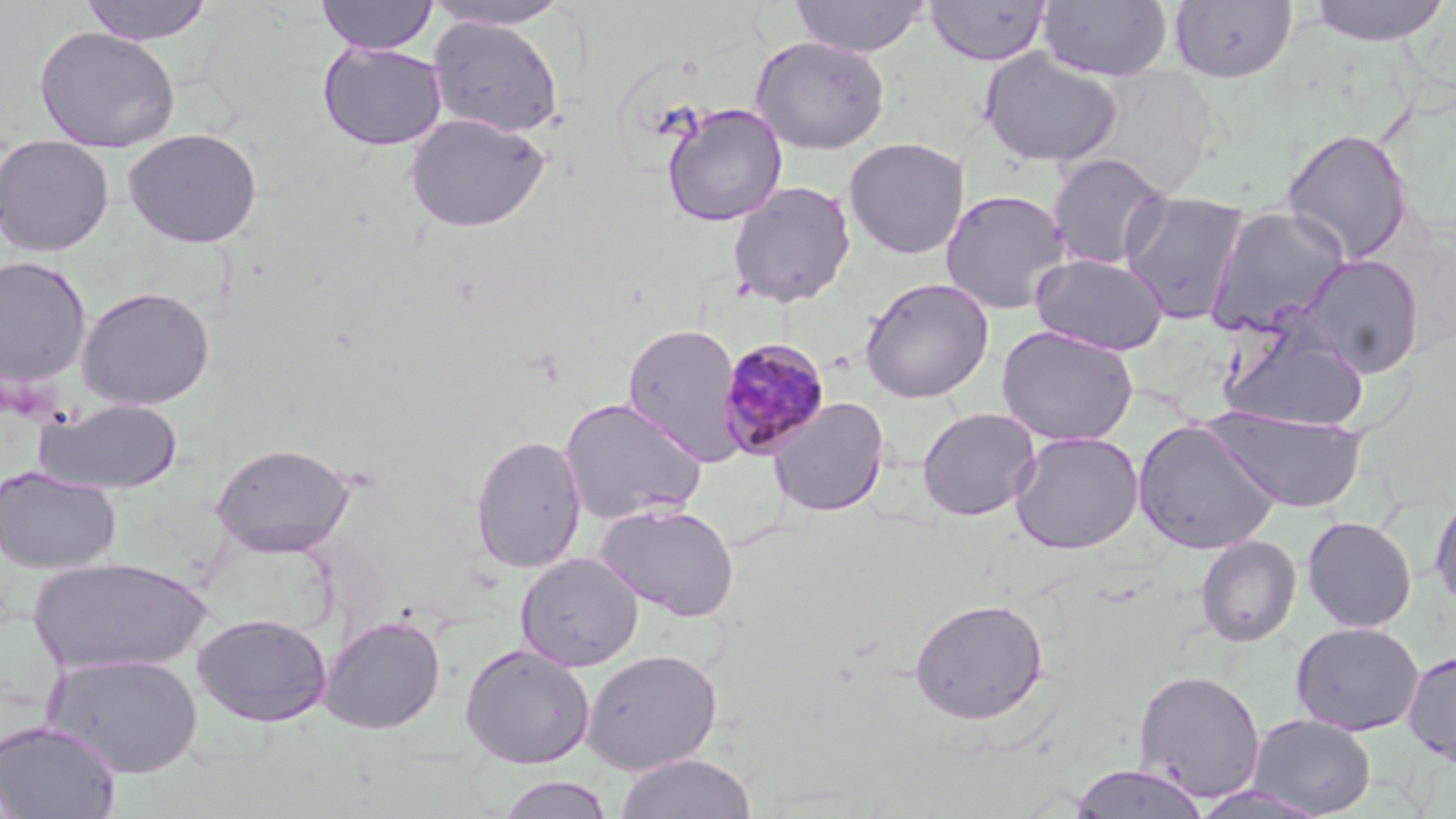
Approximate bounding boxes as (x1, y1, x2, y2) in pixels. Uninfected red blood cell locations: (79, 0, 215, 46), (315, 0, 438, 55), (789, 0, 932, 57), (1037, 0, 1173, 81), (1304, 0, 1452, 46), (420, 1, 575, 30), (924, 1, 1052, 67), (1168, 1, 1297, 83), (428, 16, 564, 138), (34, 26, 180, 152), (750, 35, 891, 154), (317, 41, 448, 151), (977, 48, 1124, 169), (661, 103, 787, 226), (404, 112, 550, 233), (122, 127, 263, 248), (1281, 128, 1414, 263), (0, 133, 114, 256), (843, 136, 969, 259), (1046, 152, 1171, 271), (727, 181, 856, 308), (939, 188, 1072, 315), (1119, 190, 1250, 324), (1205, 205, 1353, 337), (1030, 253, 1169, 356), (1299, 254, 1425, 377), (0, 256, 93, 388), (859, 276, 995, 403), (76, 286, 216, 410), (1220, 320, 1370, 431), (622, 323, 744, 463), (996, 325, 1139, 446), (559, 396, 708, 526), (37, 397, 184, 495), (767, 397, 890, 518), (916, 407, 1041, 521), (1209, 408, 1367, 514), (1133, 419, 1281, 555), (1009, 431, 1144, 554), (470, 433, 587, 573), (210, 442, 356, 557), (0, 466, 121, 574), (1429, 484, 1456, 614), (594, 501, 741, 621), (1301, 515, 1417, 632), (1195, 535, 1301, 648), (515, 552, 643, 671), (28, 555, 210, 676), (909, 597, 1048, 725), (191, 612, 333, 727), (319, 615, 446, 734), (1290, 621, 1424, 736), (459, 642, 596, 768), (581, 648, 722, 775), (1402, 650, 1456, 767), (43, 653, 203, 777), (1132, 667, 1266, 802), (1247, 713, 1376, 817), (0, 718, 122, 818), (1094, 738, 1247, 815), (614, 752, 757, 819), (1068, 763, 1211, 819), (495, 774, 616, 819), (1190, 784, 1331, 818). Plasmodium malariae-infected red blood cell locations: (717, 338, 831, 461). Slide-level diagnosis: Plasmodium malariae. Single field of view. Image is 1456×819 pixels. Thin blood film. May-Grünwald-Giemsa stain. Captured at 1000x magnification. Optical microscopy.